Report the malaria status of this cell.
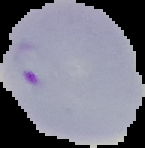
It is parasitized.

Summary:
  - Preparation: thin blood smear
  - Image type: segmented cell region on a black background
  - Image size: 145×148 pixels